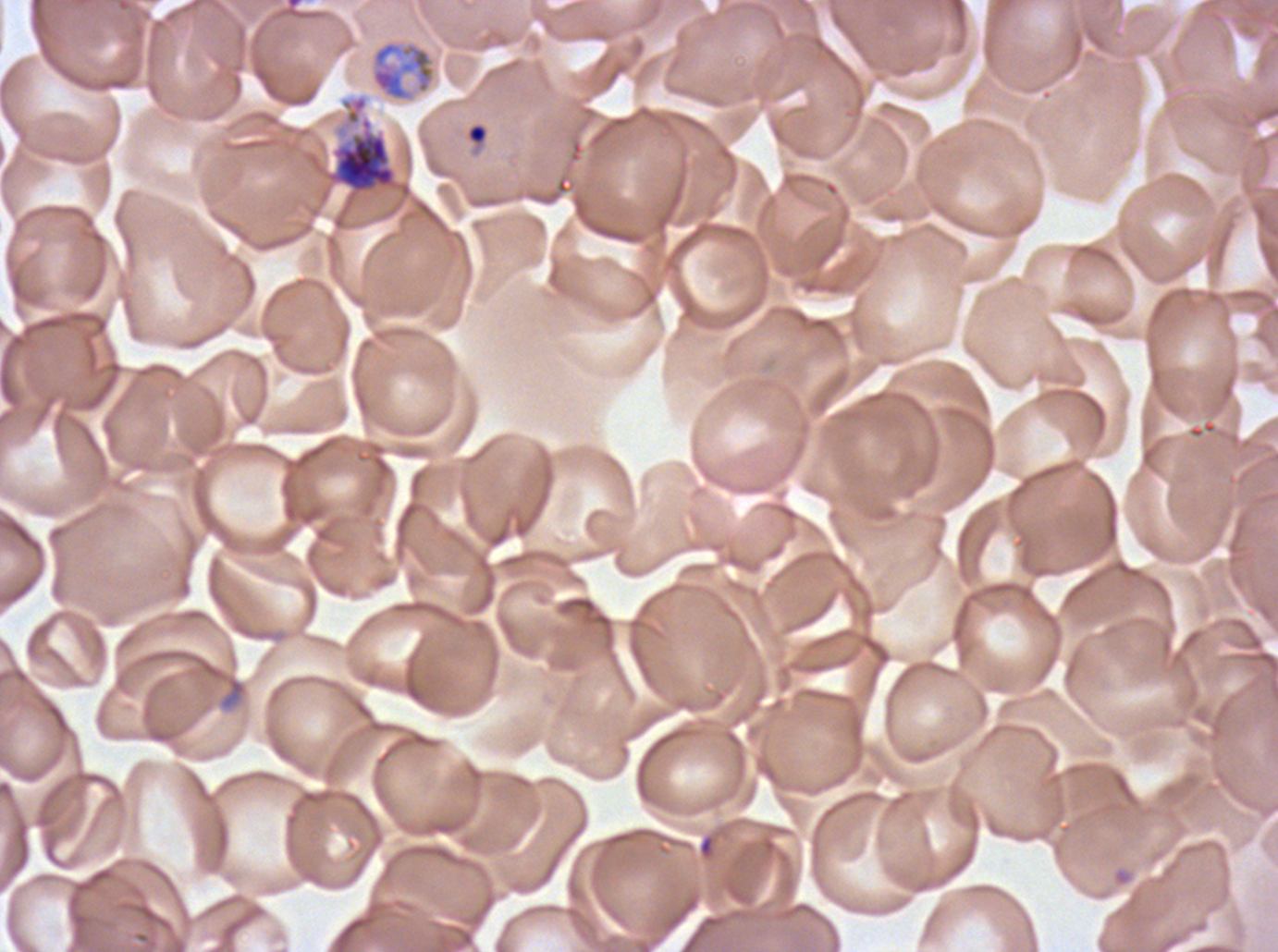

Approximate bounding rectangles given as corner coordinates in pixels from the top-left. Ring locations: (x1=469, y1=126, x2=485, y2=142). Debris locations: (x1=221, y1=676, x2=246, y2=709). Early schizont locations: (x1=326, y1=95, x2=398, y2=195). Late trophozoite locations: (x1=369, y1=38, x2=437, y2=104). Ex-vivo P. falciparum culture from a patient in The Gambia, grown for 24 to 48 hours. Thin blood smear. Image is 1278×952 pixels. Life-cycle stages observed: ring, late trophozoite, early schizont. A sub-image separated from a larger composite. Giemsa-stained preparation.